Classify this cell by malaria status.
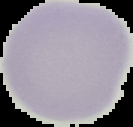
Uninfected.

Summary:
  - Image type: segmented cell region with the area outside set to black
  - Image size: 133×127 pixels
  - Preparation: thin blood film